Identify the preparation type.
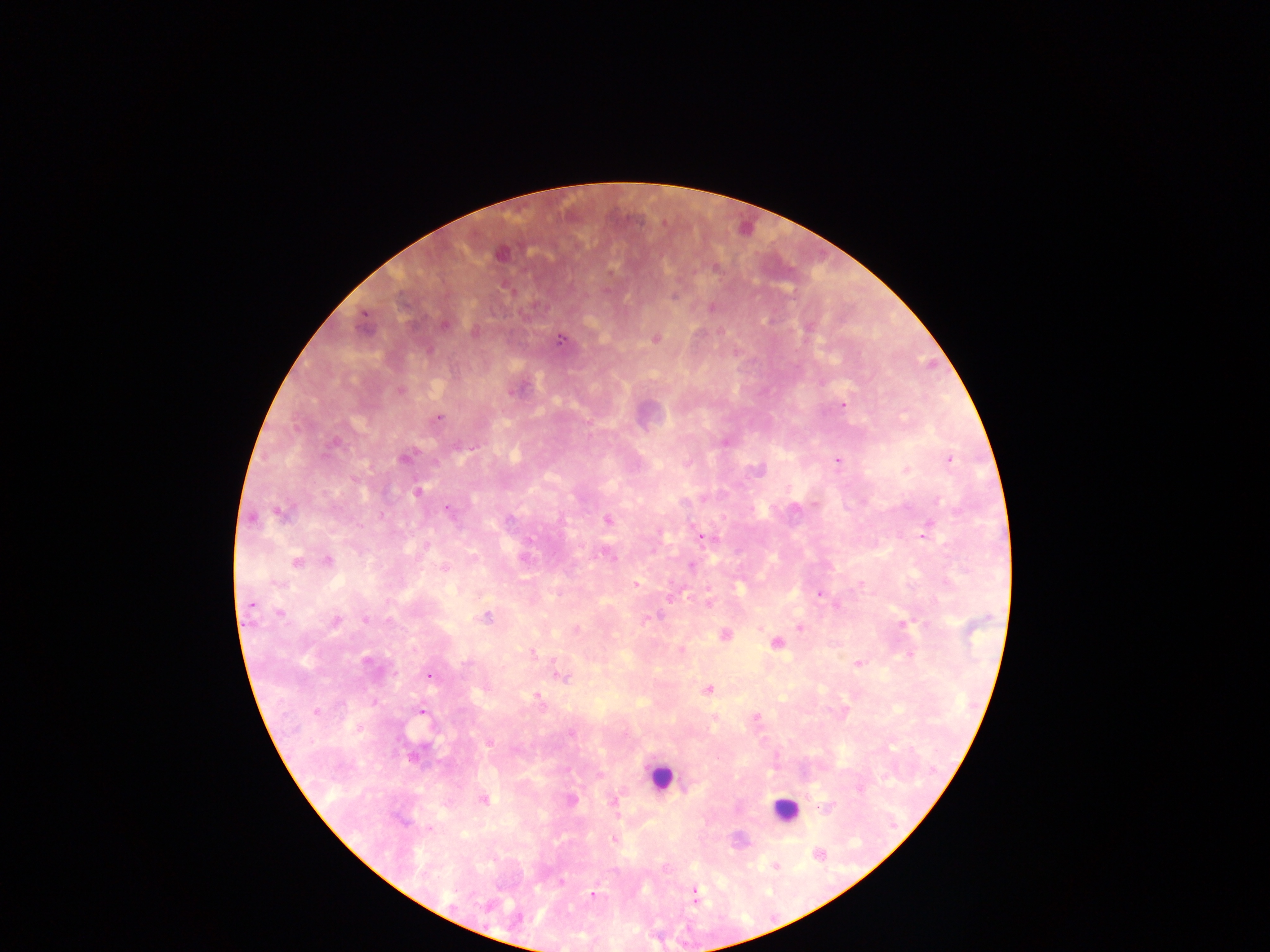
Thick blood smear.

Approximate centers as x y in pixels. Leukocyte locations: 660 776; 785 810. Plasmodium parasite locations: 500 255; 715 269; 674 295; 712 307; 445 325; 474 332; 655 339; 559 340; 400 390; 843 406; 438 418; 724 443; 333 444; 404 459; 950 459; 837 461; 687 463; 756 470; 906 470; 354 479; 417 492; 936 501; 447 509; 279 513; 253 519; 608 520; 924 536; 702 538; 530 539; 427 546; 524 559; 328 560; 295 562; 691 566; 445 568; 635 584; 709 590; 820 594; 708 603; 250 604; 279 613; 486 617; 650 618; 366 620; 336 621; 903 624; 799 627; 759 628; 576 629; 726 635; 776 643; 681 651; 533 653; 909 655; 367 661; 857 664; 429 676; 563 678; 708 689; 537 696; 422 711; 316 712; 756 716; 715 717; 359 728; 571 733; 489 743; 484 800; 572 800; 614 802; 614 840; 819 854; 775 865; 665 867; 562 882; 695 892; 592 896. One field of view. Photographed through a microscope with a mobile-phone camera. Sample from Ghana. Image is 1270×952 pixels.